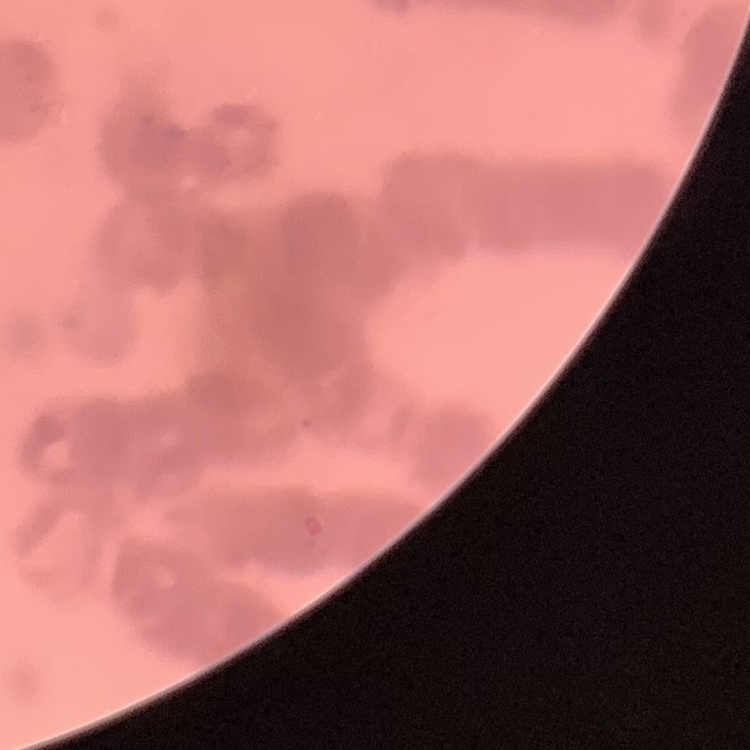

red blood cell morphology = rouleaux formation
preparation = thin blood film
stain = Field's or Giemsa
image type = square crop of a larger photomicrograph